Identify the preparation type.
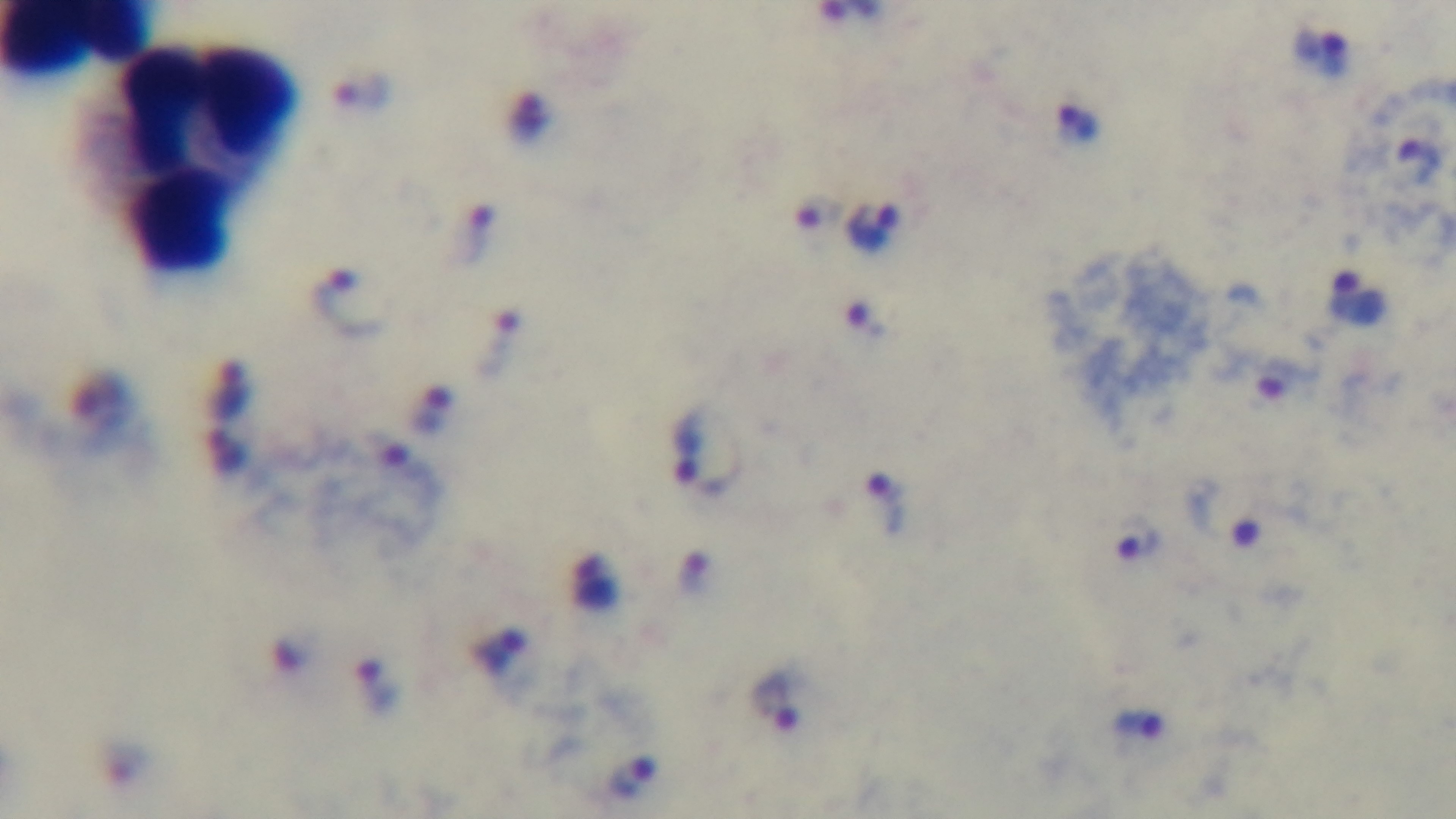

It is a thick blood film.

Summary:
  - Capture: mounted 4K digital camera
  - Malaria status: positive
  - Field of view: single
  - Stain: Giemsa
  - Modality: light microscopy
  - Objective: 100x oil immersion